Locate every blood parasite and identify its species.
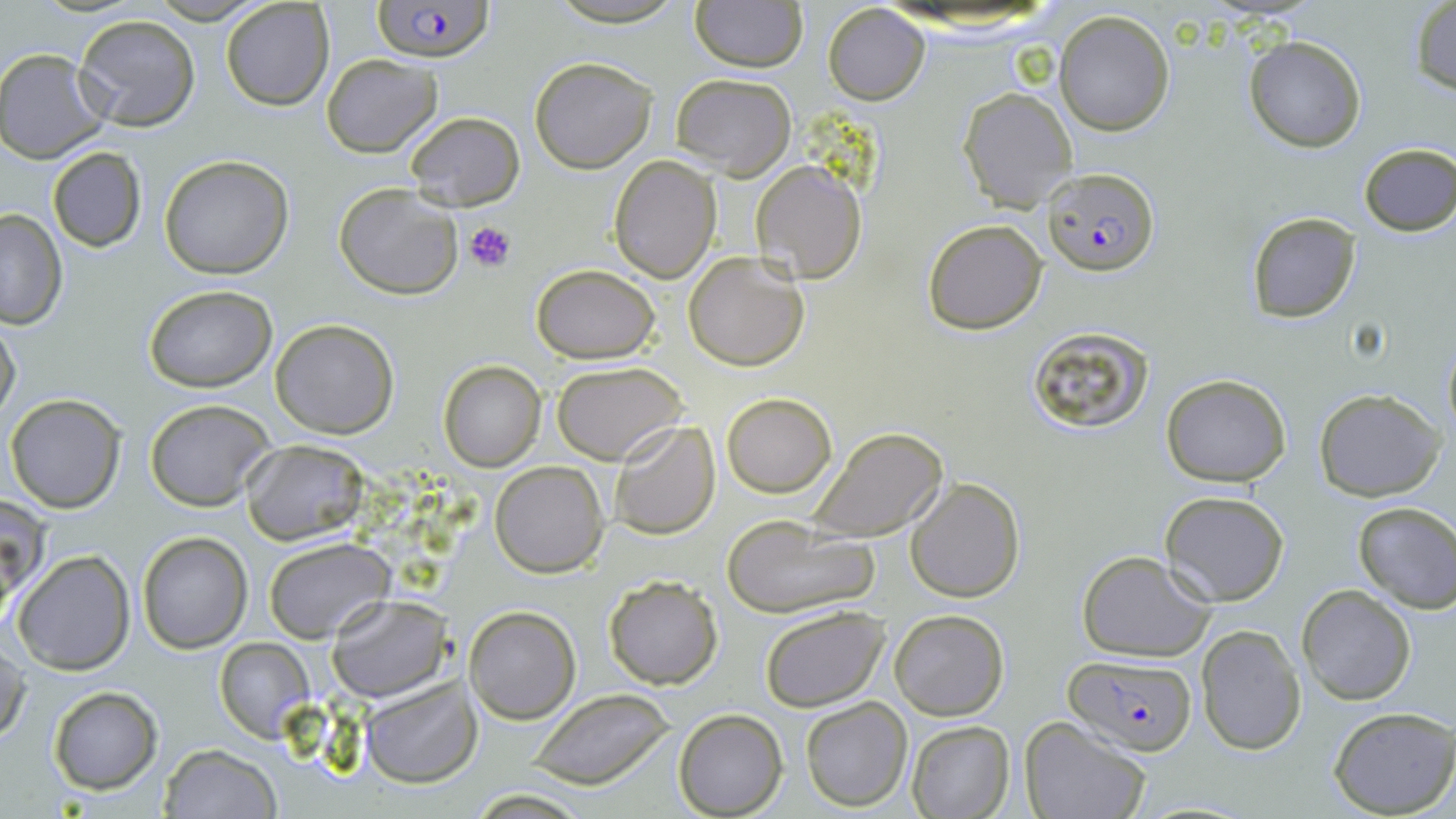

Approximate bounding boxes as [x1, y1, x2, y2] in pixels.
Plasmodium falciparum-infected red blood cells: [370, 0, 492, 62], [1042, 167, 1159, 275], [1064, 654, 1198, 756].
No Plasmodium ovale, Plasmodium malariae, Plasmodium vivax, Babesia divergens, or Trypanosoma brucei observed.

Summary:
  - Platelet locations: [462, 218, 516, 273]
  - Uninfected red blood cell locations: [690, 0, 806, 72], [1409, 1, 1455, 96], [221, 2, 334, 111], [823, 3, 929, 104], [1054, 9, 1176, 137], [72, 13, 201, 131], [1243, 35, 1367, 153], [2, 47, 110, 165], [322, 54, 443, 157], [529, 56, 656, 173], [670, 72, 796, 180], [957, 87, 1077, 212], [404, 110, 525, 211], [1357, 144, 1456, 236], [46, 146, 150, 254], [160, 155, 294, 279], [608, 156, 721, 282], [751, 161, 866, 283], [333, 184, 463, 300], [0, 209, 66, 330], [1245, 212, 1362, 322], [922, 218, 1047, 335], [683, 251, 810, 371], [530, 264, 660, 363], [144, 285, 276, 392], [0, 315, 22, 425], [270, 318, 400, 439], [1026, 325, 1157, 433], [1441, 332, 1456, 448], [437, 359, 547, 472], [552, 360, 687, 465], [1160, 373, 1291, 486], [1313, 387, 1444, 499], [721, 393, 836, 496], [5, 394, 125, 513], [144, 399, 278, 512], [608, 420, 721, 538], [808, 425, 949, 544], [242, 439, 369, 547], [490, 460, 609, 577], [905, 477, 1025, 603], [1160, 491, 1290, 606], [2, 496, 41, 618], [1351, 500, 1456, 612], [720, 514, 883, 620], [135, 532, 252, 654], [264, 537, 393, 642], [12, 550, 136, 676], [1076, 550, 1218, 662], [603, 574, 724, 690], [1296, 585, 1416, 704], [326, 593, 450, 703], [463, 605, 580, 724], [759, 605, 891, 712], [889, 608, 1009, 719], [1194, 624, 1305, 757], [1, 638, 27, 745], [214, 638, 314, 742], [358, 676, 476, 786], [47, 686, 163, 795], [528, 688, 676, 789], [800, 697, 913, 813], [1326, 707, 1456, 819], [675, 710, 788, 818], [1019, 717, 1153, 819], [905, 721, 1015, 818], [158, 744, 282, 818], [462, 788, 599, 818]
  - Slide-level diagnosis: Plasmodium falciparum
  - Field of view: one of a larger specimen
  - Preparation: thin blood film
  - Stain: May-Grünwald-Giemsa
  - Image size: 1456×819 pixels
  - Modality: optical microscopy
  - Magnification: 1000x